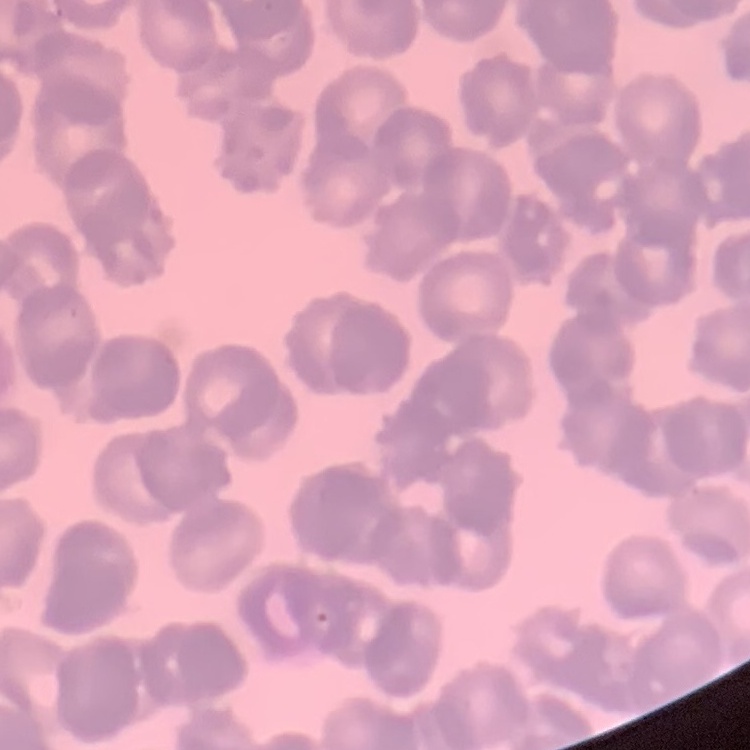
Summary:
  - Erythrocyte morphology: rouleaux formation
  - Stain: Field's or Giemsa
  - Image type: one tile cut from a larger photomicrograph
  - Preparation: thin blood film